Point out each Plasmodium parasite.
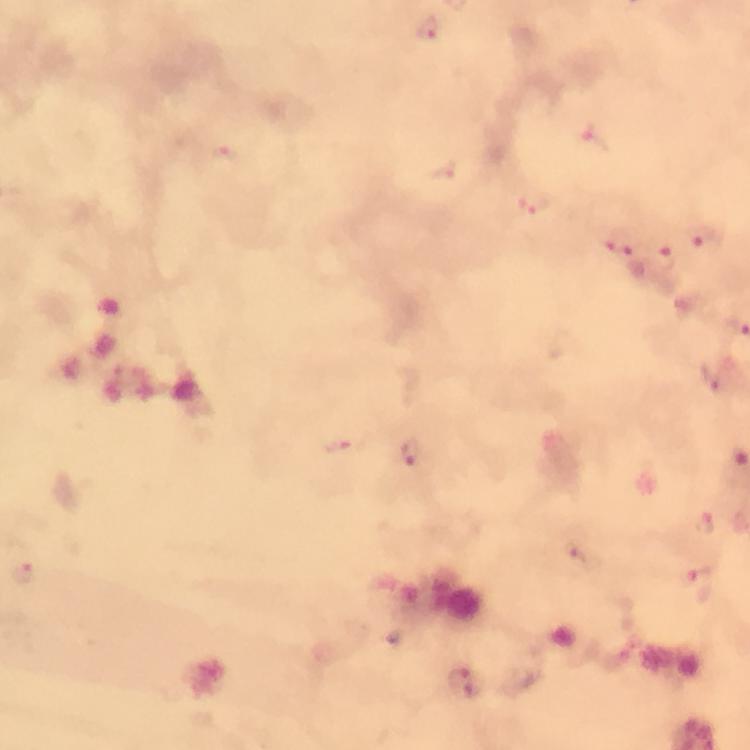

Approximate centers as (x, y) in pixels.
Plasmodium parasites: (429, 26), (593, 136), (222, 159), (441, 172), (537, 203), (707, 240), (620, 244), (665, 261), (413, 453), (578, 558), (21, 574), (697, 582), (463, 682).

capture = smartphone mounted on the microscope
stain = Giemsa
image size = 750×750 pixels
magnification = 100x
cropped from = one field of view
immersion oil = applied
context = from a malaria diagnostic workup
preparation = thick blood smear